Identify the preparation type.
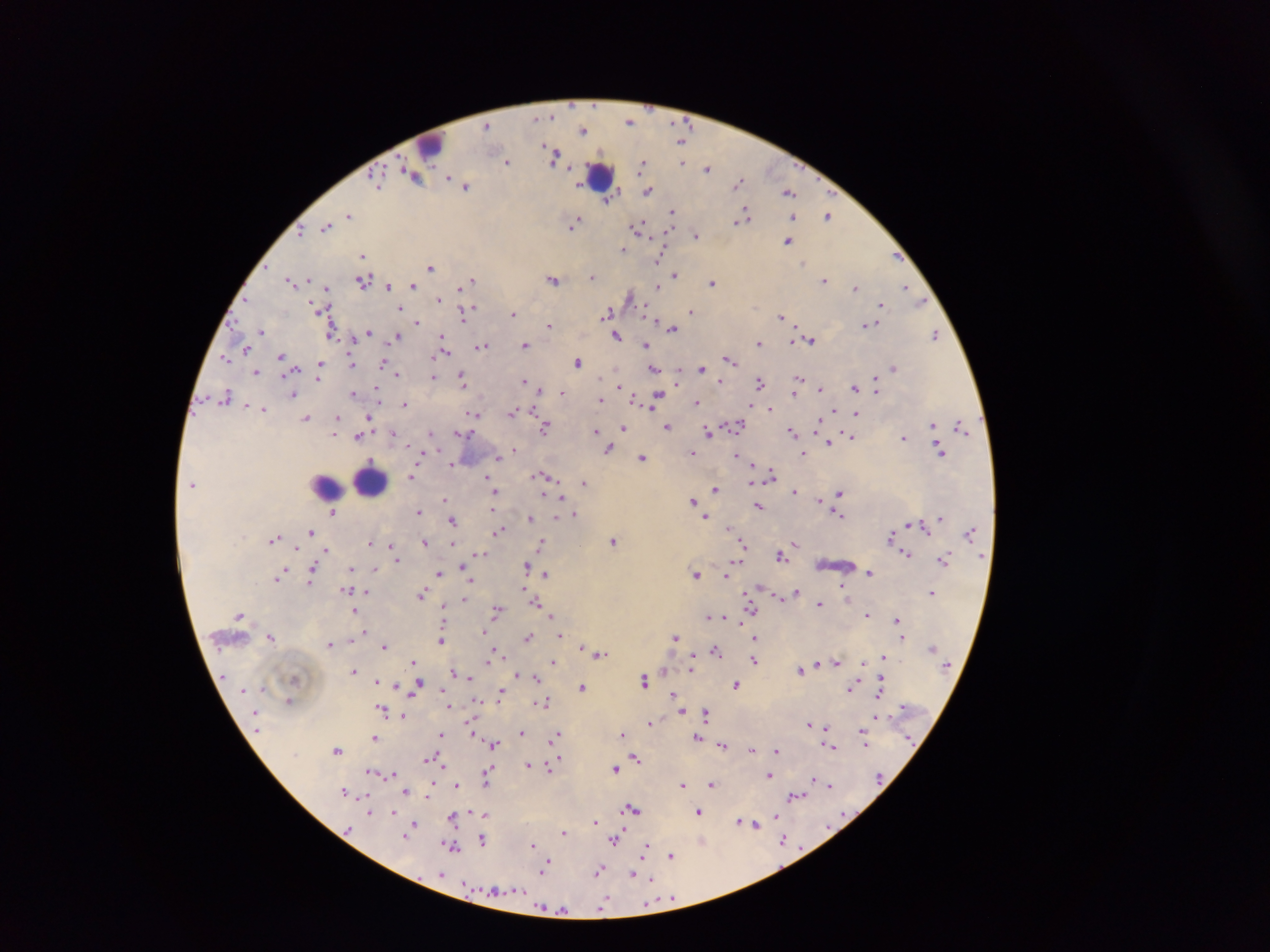

Thick blood smear.

country: Ghana
image_size: 1270×952 pixels
plasmodium_parasite_locations: 'approximate centers as x y in pixels: 630 121; 488 124; 583 129; 682 141; 555 155; 507 161; 683 162; 644 164; 708 168; 414 175; 377 181; 739 182; 465 185; 649 191; 790 193; 608 200; 673 210; 745 215; 828 215; 348 216; 793 217; 575 222; 327 226; 638 226; 697 235; 789 241; 623 249; 897 255; 363 256; 660 258; 431 265; 593 275; 674 275; 554 279; 473 280; 292 281; 363 281; 824 281; 713 282; 414 284; 389 285; 658 286; 906 287; 327 288; 855 288; 630 296; 439 298; 882 304; 400 307; 322 310; 513 312; 463 313; 608 313; 692 313; 782 316; 417 321; 869 324; 549 326; 671 327; 261 331; 331 331; 370 332; 935 334; 617 335; 398 336; 355 337; 442 338; 811 339; 795 340; 759 343; 525 344; 483 346; 645 346; 246 349; 445 352; 282 356; 224 358; 729 359; 351 361; 385 362; 578 362; 321 364; 702 367; 893 367; 295 369; 654 369; 256 371; 397 374; 434 375; 799 376; 319 377; 464 378; 677 378; 525 381; 720 381; 877 381; 760 382; 620 385; 855 387; 820 388; 378 390; 795 392; 354 393; 561 393; 293 395; 226 396; 657 396; 636 398; 600 399; 696 401; 405 403; 751 404; 263 408; 535 408; 770 409; 836 409; 513 412; 476 413; 857 413; 370 415; 307 417; 337 417; 737 423; 819 423; 933 425; 668 426; 961 426; 545 427; 623 427; 597 430; 793 430; 708 431; 432 432; 394 433; 461 433; 336 434; 358 436; 851 436; 903 437; 829 441; 610 448; 514 449; 939 449; 693 453; 737 455; 804 455; 497 457; 642 458; 750 463; 452 464; 753 472; 771 473; 544 475; 412 476; 488 480; 584 482; 751 482; 492 484; 716 488; 495 491; 795 491; 839 493; 544 494; 561 496; 445 500; 821 500; 694 502; 759 507; 418 510; 494 510; 333 512; 574 513; 841 516; 705 517; 558 518; 940 518; 530 519; 452 520; 917 525; 729 527; 499 531; 971 531; 312 532; 891 536; 275 539; 613 540; 370 542; 424 542; 796 542; 453 543; 543 543; 743 543; 299 548; 393 549; 327 550; 481 553; 906 554; 781 556; 396 560; 944 560; 739 561; 465 566; 527 566; 351 567; 312 568; 376 568; 696 573; 871 573; 440 574; 545 574; 282 575; 727 575; 471 581; 311 582; 844 586; 347 588; 526 589; 366 590; 797 592; 931 592; 422 593; 779 595; 464 600; 536 601; 819 603; 751 606; 444 608; 355 609; 497 609; 241 614; 552 614; 868 615; 709 616; 726 616; 897 619; 741 621; 364 631; 485 631; 358 633; 560 635; 528 636; 676 636; 272 637; 755 637; 900 638; 442 640; 329 645; 384 645; 582 646; 498 649; 716 650; 601 653; 883 656; 755 660; 414 661; 552 661; 837 661; 488 662; 862 662; 817 663; 692 668; 801 669; 354 670; 664 670; 454 672; 517 675; 470 677; 536 677; 377 680; 644 680; 880 680; 418 683; 736 684; 396 685; 583 687; 443 688; 851 688; 501 692; 674 694; 677 699; 478 700; 543 700; 290 701; 449 705; 381 710; 681 710; 705 714; 403 715; 876 715; 472 722; 651 722; 810 724; 827 727; 472 731; 521 732; 623 732; 440 734; 863 734; 556 735; 375 737; 698 737; 866 742; 494 744; 723 744; 831 745; 752 748; 338 749; 777 750; 431 756; 559 757; 635 757; 427 759; 553 762; 529 764; 549 768; 615 768; 372 772; 488 772; 392 773; 769 775; 488 778; 814 779; 432 782; 712 783; 683 784; 457 785; 829 785; 406 790; 345 791; 796 795; 428 797; 632 808; 371 812; 699 812; 394 813; 472 813; 486 814; 775 815; 453 817; 595 821; 741 822; 415 823; 755 823; 564 832; 406 835; 482 839; 784 839; 616 840; 702 841; 534 844; 452 846; 645 850; 672 855; 549 864; 545 868; 599 871; 633 875; 651 879; 670 899; 606 901; 602 906; 564 909'
field_of_view: single
capture: mobile-phone photograph through a microscope
leukocyte_locations: 'approximate centers as x y in pixels: 430 143; 601 174; 369 480; 327 485'